Comment on the morphology of the erythrocytes.
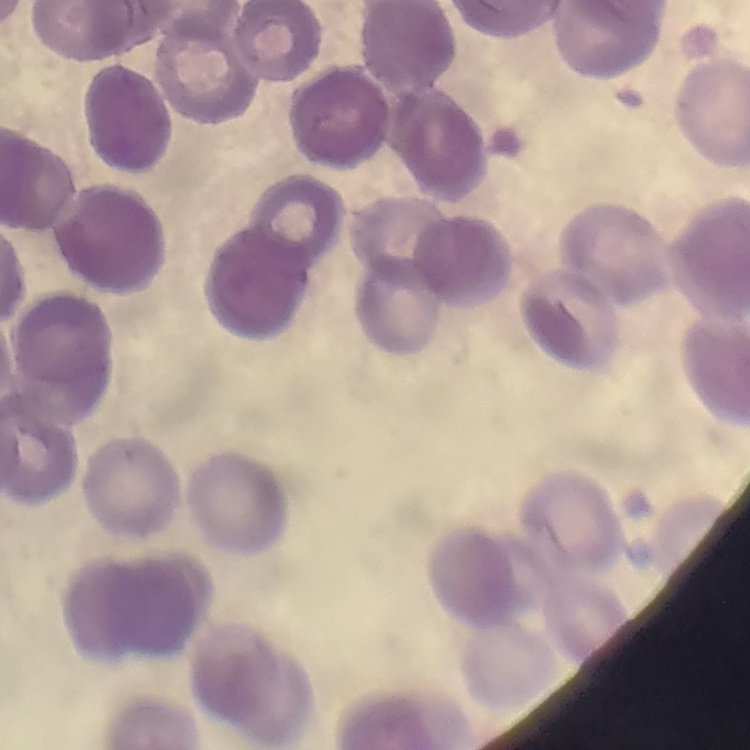
Rouleaux formation.

Stained with either Field's or Giemsa. Thin blood film. One tile cut from a larger photomicrograph.